Identify the parasite.
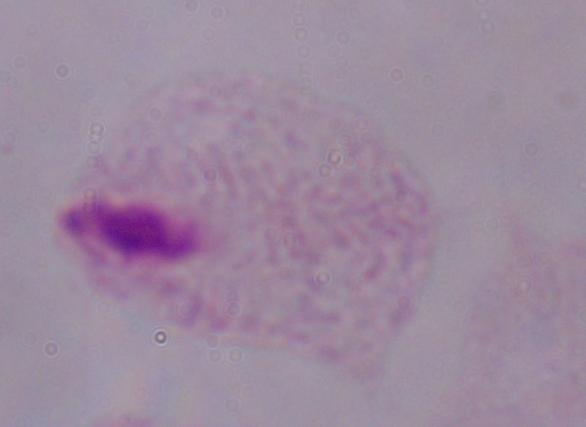

This is a trichomonad.

Summary:
  - Modality: micrograph
  - Magnification: 1000x